Identify the cell.
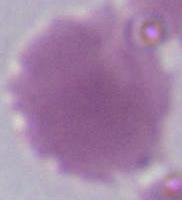

This is an erythrocyte.

Summary:
  - Modality: photomicrograph
  - Magnification: 1000x